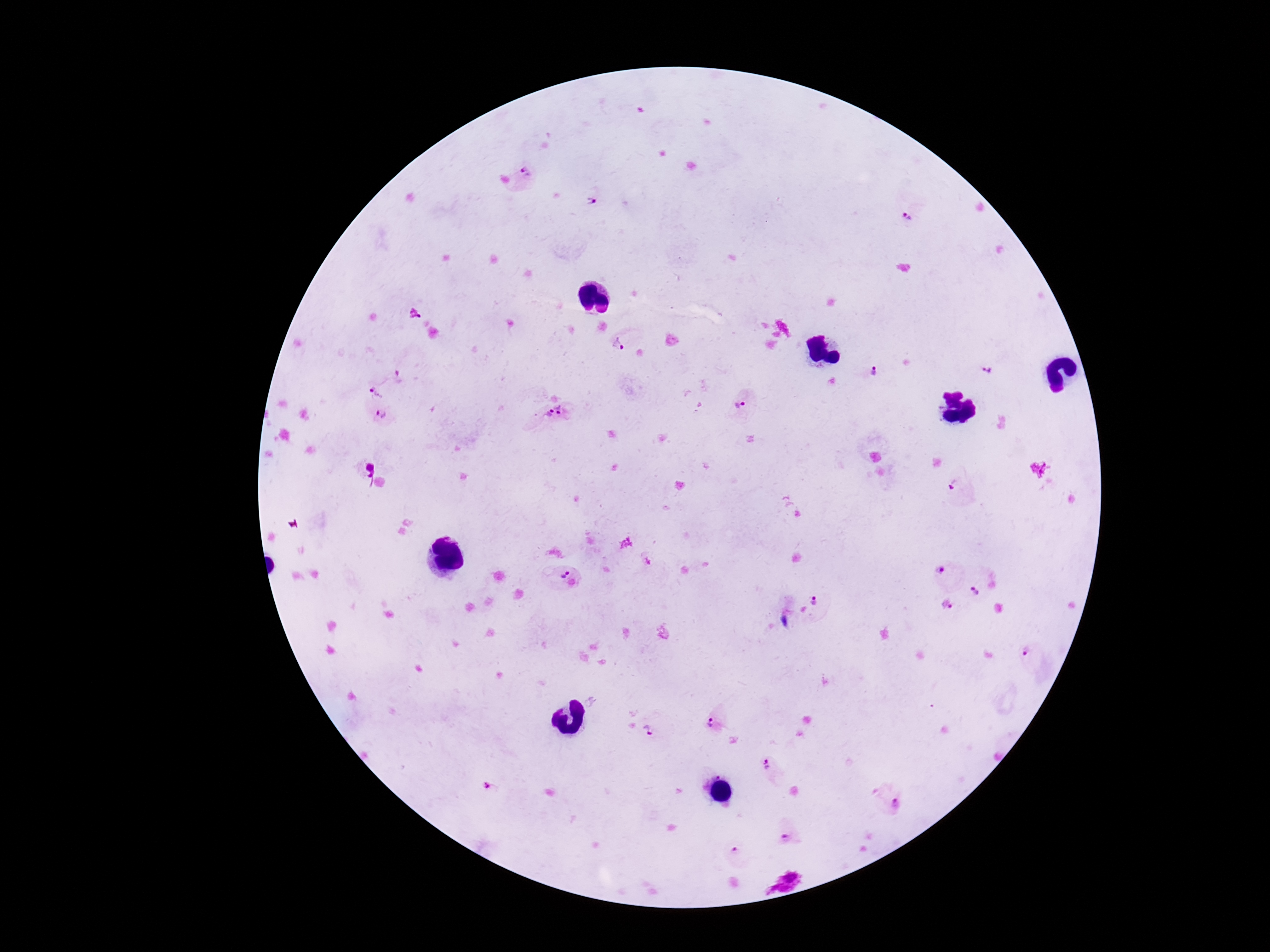

{
  "plasmodium_parasite_locations": "approximate centers as [x, y] in pixels: [530, 174], [593, 196], [626, 339], [991, 361], [869, 375], [400, 377], [377, 391], [743, 403], [566, 411], [382, 415], [542, 417], [961, 490], [556, 572], [942, 573], [983, 584], [811, 605], [949, 608], [1026, 650], [718, 721], [654, 731], [771, 770], [491, 788], [895, 800], [789, 832], [739, 850]",
  "patient_malaria_status": "positive",
  "stain": "Giemsa",
  "capture": "smartphone camera through the microscope eyepiece",
  "preparation": "thick blood smear",
  "magnification": "100x",
  "image_size": "1270×952 pixels",
  "field_of_view": "one from this slide"
}